Identify the blood parasite species.
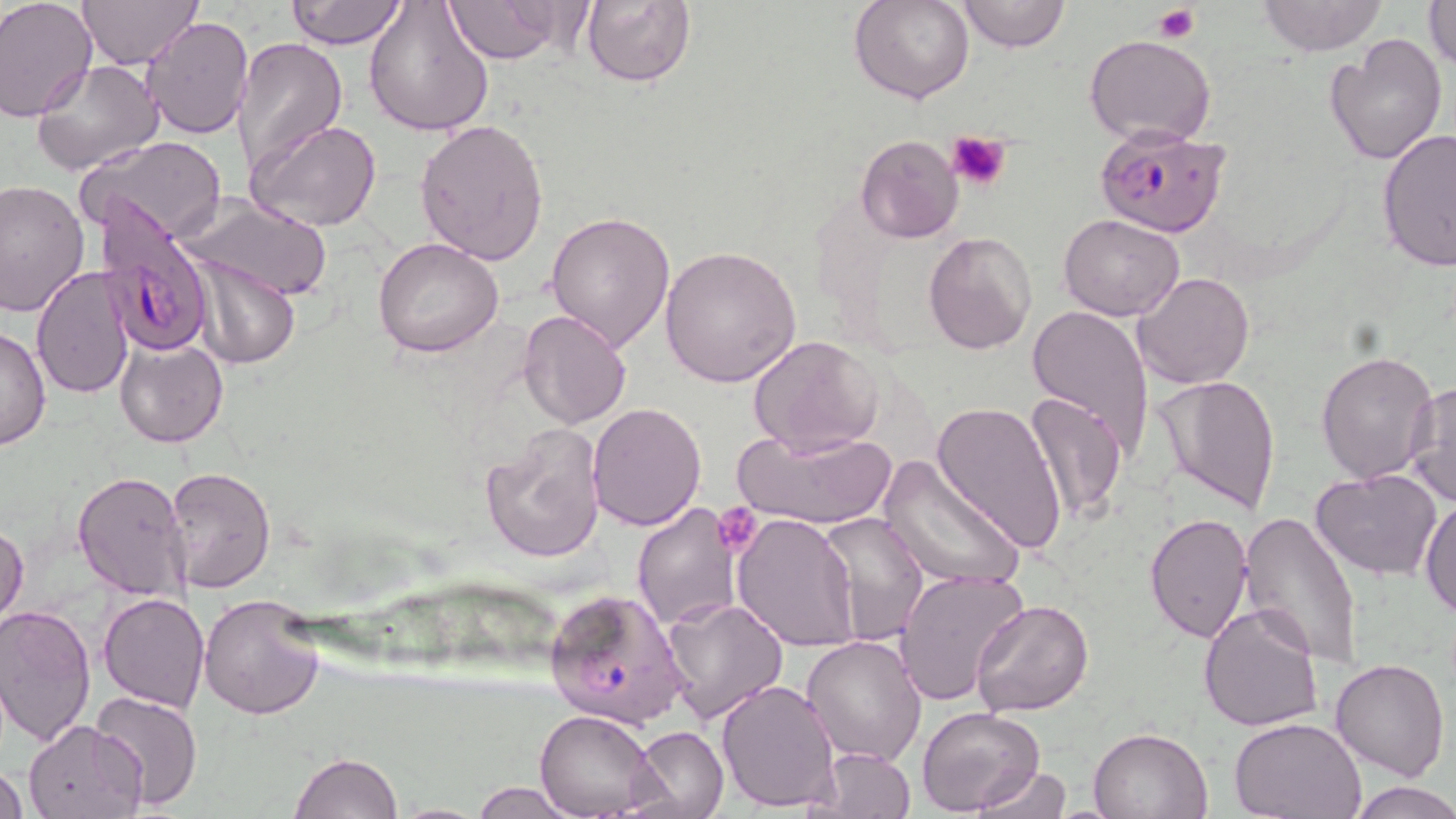
Plasmodium falciparum.

Approximate bounding boxes as named x1/y1/x2/y2 corners in pixels. Uninfected red blood cell locations: (x1=0, y1=0, x2=96, y2=121), (x1=78, y1=0, x2=203, y2=69), (x1=285, y1=0, x2=407, y2=49), (x1=363, y1=0, x2=495, y2=137), (x1=442, y1=0, x2=577, y2=64), (x1=850, y1=0, x2=975, y2=105), (x1=958, y1=0, x2=1070, y2=53), (x1=1257, y1=0, x2=1385, y2=56), (x1=1424, y1=0, x2=1456, y2=68), (x1=580, y1=1, x2=697, y2=88), (x1=140, y1=18, x2=254, y2=140), (x1=1083, y1=34, x2=1216, y2=147), (x1=1324, y1=34, x2=1448, y2=167), (x1=231, y1=37, x2=348, y2=170), (x1=31, y1=59, x2=164, y2=178), (x1=248, y1=118, x2=383, y2=233), (x1=416, y1=120, x2=550, y2=267), (x1=1376, y1=127, x2=1456, y2=271), (x1=854, y1=134, x2=965, y2=243), (x1=79, y1=136, x2=229, y2=242), (x1=1, y1=181, x2=92, y2=320), (x1=177, y1=191, x2=332, y2=301), (x1=545, y1=210, x2=676, y2=351), (x1=1060, y1=214, x2=1184, y2=322), (x1=921, y1=230, x2=1037, y2=355), (x1=374, y1=238, x2=503, y2=357), (x1=658, y1=244, x2=803, y2=387), (x1=186, y1=255, x2=300, y2=368), (x1=31, y1=265, x2=135, y2=399), (x1=1134, y1=271, x2=1255, y2=389), (x1=1029, y1=305, x2=1154, y2=454), (x1=518, y1=309, x2=631, y2=429), (x1=1, y1=323, x2=49, y2=452), (x1=748, y1=335, x2=881, y2=457), (x1=116, y1=339, x2=228, y2=448), (x1=1315, y1=349, x2=1440, y2=485), (x1=1152, y1=373, x2=1281, y2=515), (x1=1406, y1=379, x2=1456, y2=510), (x1=1024, y1=391, x2=1128, y2=526), (x1=931, y1=399, x2=1067, y2=555), (x1=587, y1=403, x2=708, y2=531), (x1=476, y1=422, x2=605, y2=562), (x1=732, y1=424, x2=898, y2=532), (x1=875, y1=457, x2=1027, y2=593), (x1=165, y1=465, x2=276, y2=594), (x1=73, y1=470, x2=195, y2=601), (x1=1310, y1=470, x2=1442, y2=580), (x1=1420, y1=495, x2=1455, y2=619), (x1=631, y1=503, x2=742, y2=631), (x1=1142, y1=511, x2=1252, y2=645), (x1=1238, y1=511, x2=1365, y2=666), (x1=731, y1=512, x2=860, y2=651), (x1=815, y1=512, x2=928, y2=649), (x1=1, y1=519, x2=28, y2=633), (x1=894, y1=567, x2=1029, y2=708), (x1=98, y1=593, x2=210, y2=711), (x1=198, y1=594, x2=324, y2=720), (x1=659, y1=594, x2=787, y2=724), (x1=971, y1=599, x2=1093, y2=716), (x1=0, y1=601, x2=97, y2=747), (x1=1197, y1=603, x2=1323, y2=734), (x1=802, y1=634, x2=928, y2=766), (x1=1330, y1=658, x2=1450, y2=781), (x1=716, y1=679, x2=840, y2=813), (x1=91, y1=689, x2=203, y2=810), (x1=916, y1=706, x2=1045, y2=815), (x1=536, y1=711, x2=660, y2=818), (x1=1232, y1=716, x2=1367, y2=819), (x1=23, y1=720, x2=147, y2=817), (x1=632, y1=726, x2=728, y2=819), (x1=1089, y1=727, x2=1212, y2=818), (x1=808, y1=745, x2=918, y2=817), (x1=289, y1=753, x2=401, y2=819), (x1=0, y1=765, x2=30, y2=817), (x1=972, y1=765, x2=1071, y2=819), (x1=1347, y1=778, x2=1456, y2=818), (x1=468, y1=782, x2=583, y2=817). Plasmodium falciparum-infected red blood cell locations: (x1=1095, y1=125, x2=1228, y2=237), (x1=89, y1=200, x2=216, y2=355), (x1=542, y1=585, x2=688, y2=728). Platelet locations: (x1=1155, y1=6, x2=1200, y2=42), (x1=947, y1=131, x2=1011, y2=192), (x1=715, y1=508, x2=763, y2=555). Image is 1456×819 pixels. 1000x magnification. One field of a larger specimen. Thin blood film. May-Grünwald-Giemsa-stained preparation. Light microscopy.